State the preparation type.
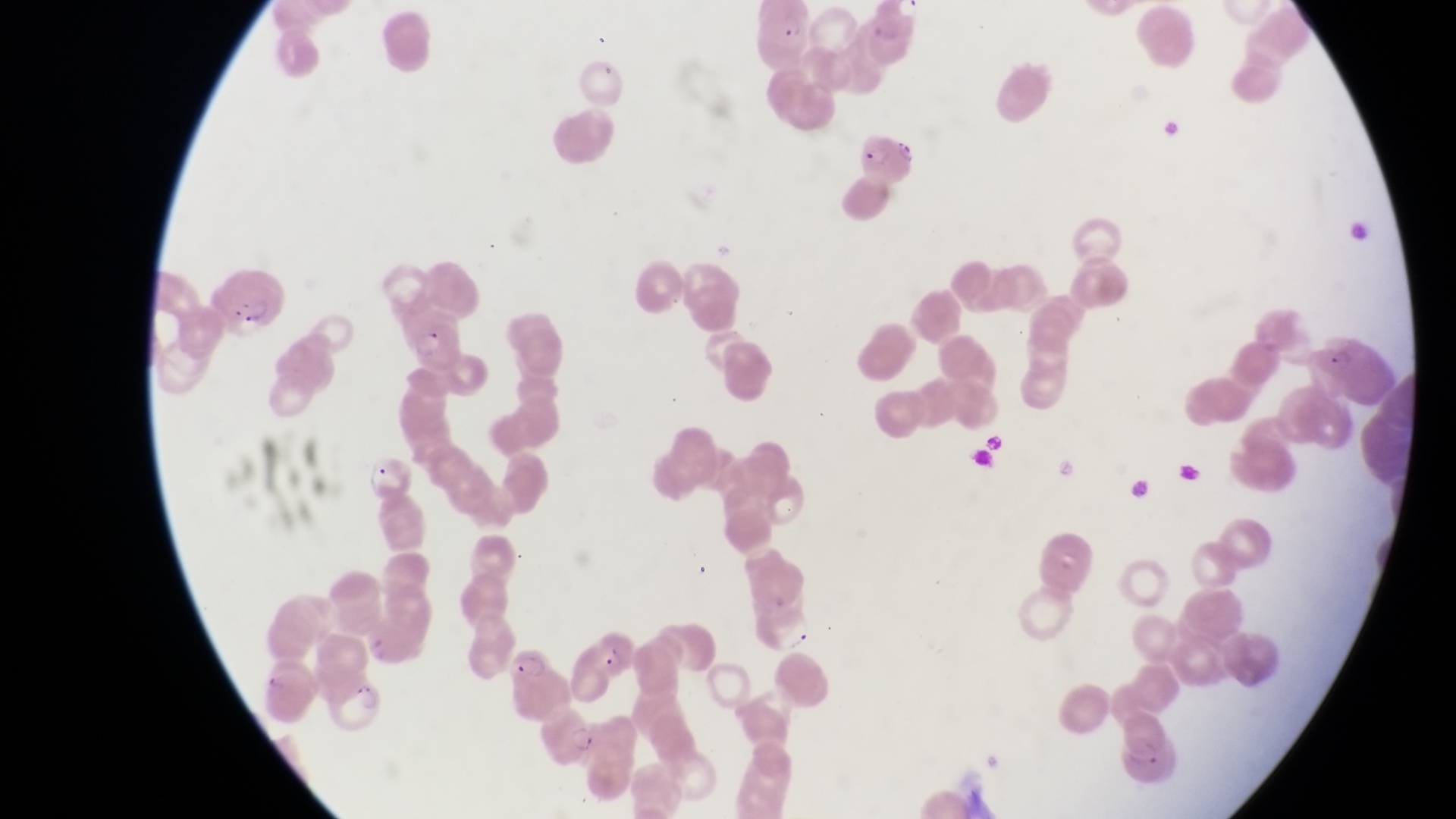

Thin blood smear.

Approximate bounding boxes as left top right bottom in pixels.
Summary:
  - Parasitised red blood cell locations: 758 3 818 62; 864 125 919 189; 214 274 286 332; 397 306 463 370; 1321 325 1390 407; 364 444 417 508; 581 621 640 682; 504 637 560 708; 333 677 386 736; 536 704 600 764
  - Magnification: 1000x
  - Field of view: single
  - Capture: smartphone photograph through the eyepiece of an Olympus CX-23 microscope
  - Country: Uganda
  - Image size: 1456×819 pixels